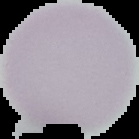
From a thin blood film. Segmented cell region on a black background. Image is 139×139 pixels. Result: no Plasmodium parasites seen.